State the preparation type.
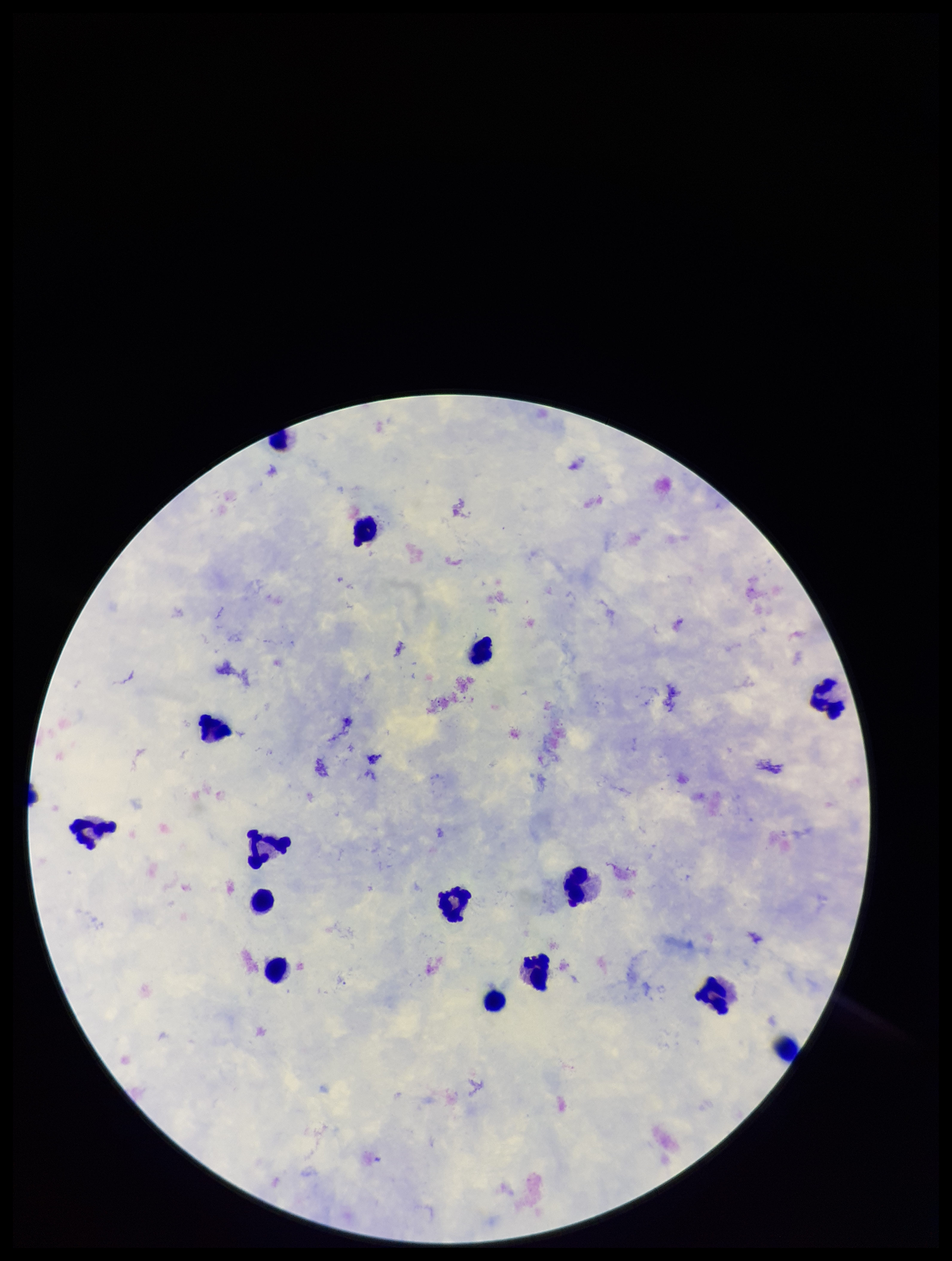
It is a thick blood smear.

field of view = one from this slide
Plasmodium parasites = none identified
parasite count = 0
image size = 952×1261 pixels
species reported for this patient = Plasmodium falciparum
patient malaria status = infected
capture = smartphone photograph through the microscope eyepiece
stain = Giemsa
leukocyte count = 15